Assess this cell for malaria.
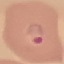
Parasitized.

preparation: thin blood smear
image_type: automatically extracted cell patch, resized to 64 × 64 pixels
stain: Giemsa
capture: smartphone camera at the microscope eyepiece